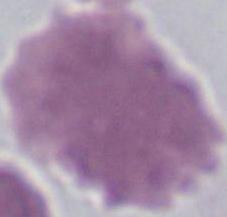
Summary:
  - Modality: micrograph
  - Magnification: 1000x
  - Identification: red blood cell